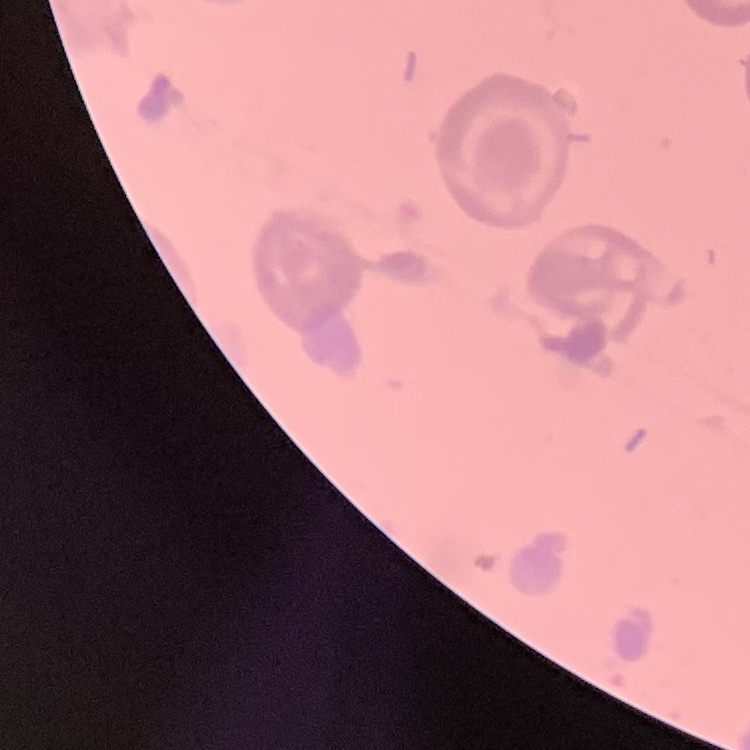

The red blood cells show no rouleaux formation. Stained with either Field's or Giemsa. Thin blood smear. One tile cut from a larger photomicrograph.